State which parasite is depicted.
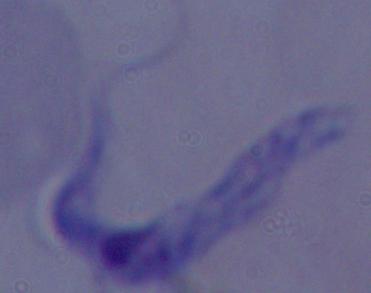
A trypanosome.

Summary:
  - Magnification: 1000x
  - Modality: photomicrograph